Describe the morphology of the erythrocytes.
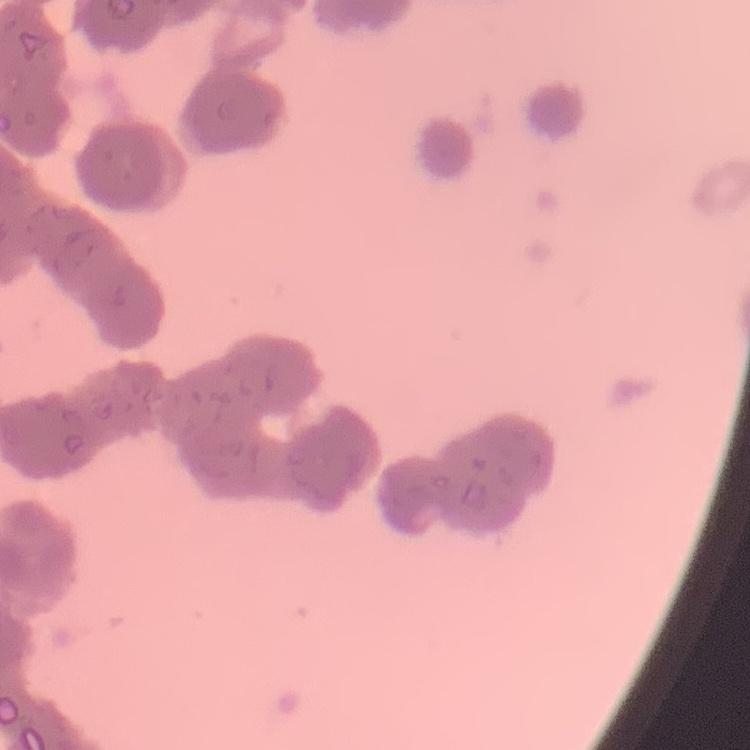

They show rouleaux formation.

Summary:
  - Image type: one tile cut from a larger photomicrograph
  - Stain: Field's or Giemsa
  - Preparation: thin blood film